Name the parasite shown.
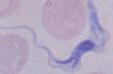
A trypanosome.

Summary:
  - Modality: photomicrograph
  - Magnification: 1000x